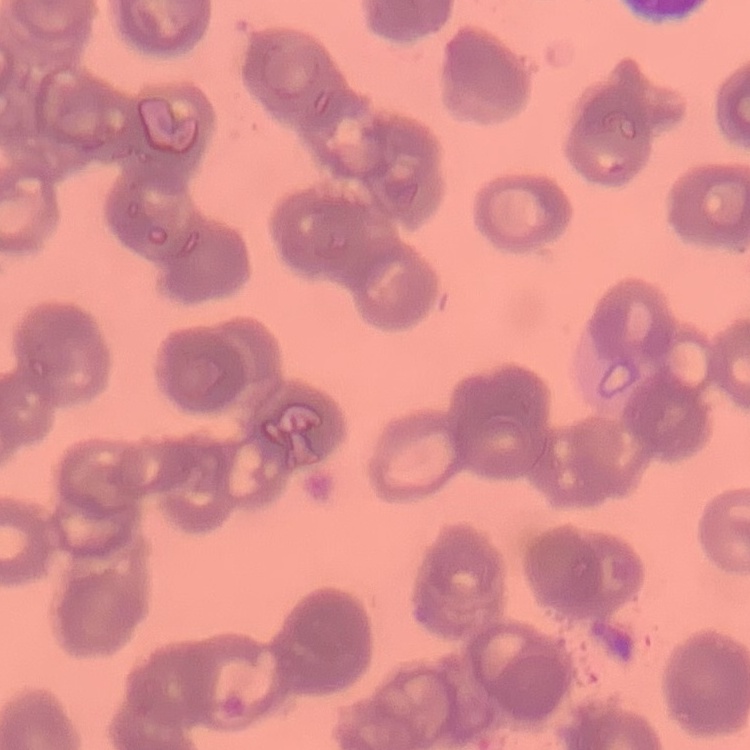
erythrocyte_morphology: rouleaux formation
stain: Field's or Giemsa
image_type: one tile cut from a larger photomicrograph
preparation: thin peripheral smear